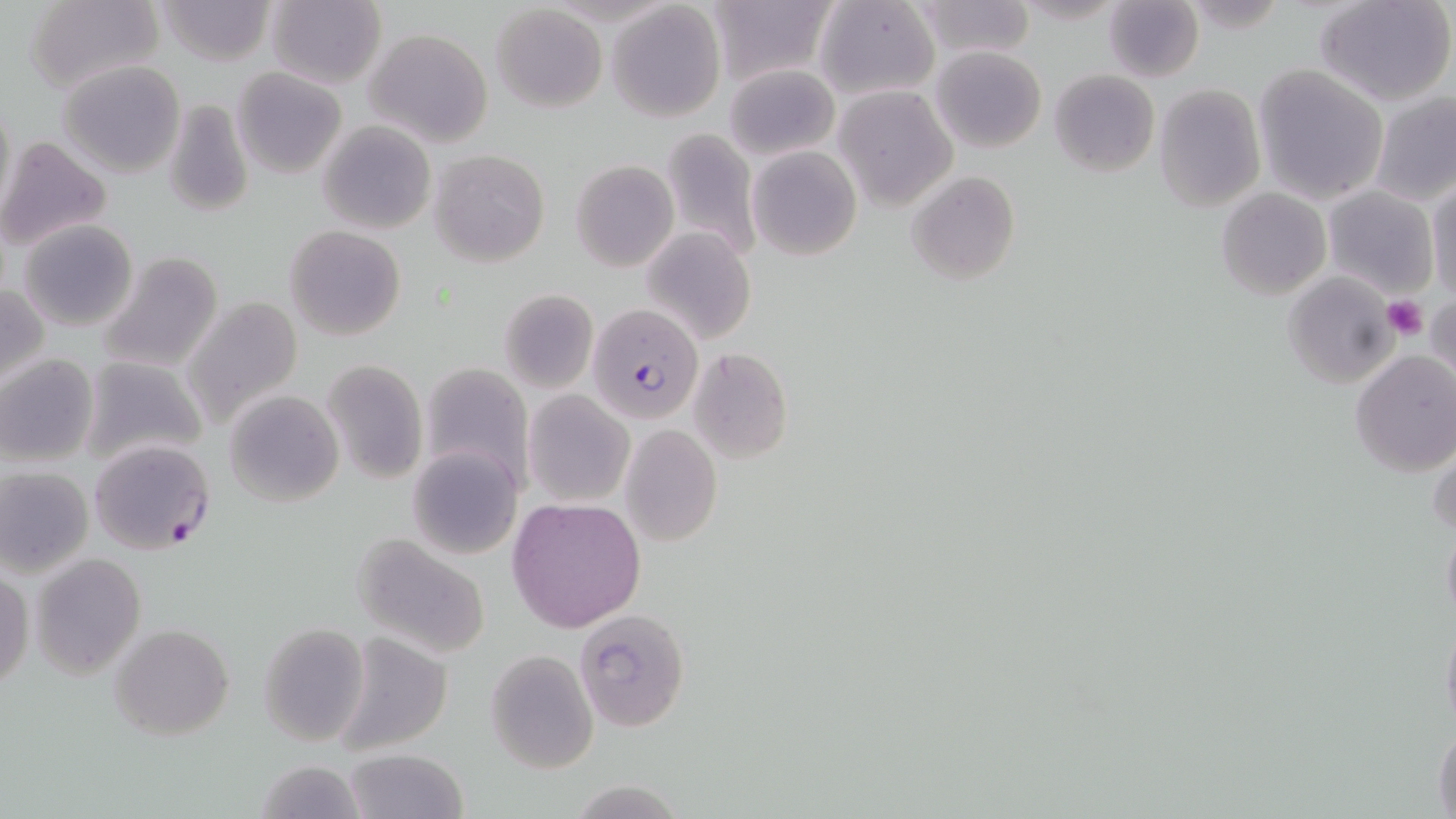
slide-level diagnosis = Plasmodium falciparum
platelet locations = approximate bounding boxes as (x1,y1)-(x2,y2) corner pairs in pixels: (1383,295)-(1427,341)
stain = May-Grünwald-Giemsa
modality = light microscopy
magnification = 1000x
field of view = single
uninfected red blood cell locations = approximate bounding boxes as (x1,y1)-(x2,y2) corner pairs in pixels: (155,0)-(275,67), (705,0)-(837,86), (816,0)-(941,103), (1011,0)-(1127,25), (1314,0)-(1456,108), (26,1)-(164,93), (265,1)-(386,87), (914,1)-(1035,58), (606,2)-(725,121), (1103,2)-(1203,81), (492,5)-(607,113), (364,29)-(494,148), (931,46)-(1047,153), (58,60)-(185,177), (725,64)-(839,161), (1253,65)-(1388,203), (232,66)-(348,180), (1050,69)-(1158,177), (1154,83)-(1265,212), (835,86)-(958,210), (1370,93)-(1456,207), (1,96)-(16,222), (162,98)-(254,220), (318,120)-(436,235), (660,127)-(760,263), (0,135)-(113,252), (746,147)-(862,261), (430,149)-(551,268), (570,160)-(678,271), (905,171)-(1020,283), (1427,179)-(1455,300), (1323,185)-(1439,300), (1216,188)-(1331,300), (17,220)-(140,333), (285,226)-(406,342), (642,228)-(756,348), (97,250)-(223,374), (1283,272)-(1397,388), (0,282)-(48,392), (498,289)-(598,393), (1427,291)-(1454,388), (183,296)-(304,431), (687,347)-(793,463), (1350,350)-(1456,477), (0,354)-(99,467), (79,356)-(207,471), (322,358)-(427,485), (419,361)-(535,490), (225,390)-(343,509), (523,390)-(634,508), (620,423)-(723,549), (1429,433)-(1455,543), (407,447)-(522,560), (0,467)-(93,577), (506,497)-(646,631), (1441,521)-(1456,628), (353,533)-(491,661), (31,553)-(146,678), (0,570)-(32,693), (574,608)-(691,732), (1440,615)-(1456,738), (110,623)-(234,739), (258,624)-(370,744), (331,633)-(453,755), (484,652)-(597,774), (1432,721)-(1456,819), (343,748)-(469,819), (256,756)-(366,819), (566,780)-(686,817)
Plasmodium falciparum-infected red blood cell locations = approximate bounding boxes as (x1,y1)-(x2,y2) corner pairs in pixels: (588,302)-(704,425), (87,438)-(215,554)
image size = 1456×819 pixels
preparation = thin blood smear